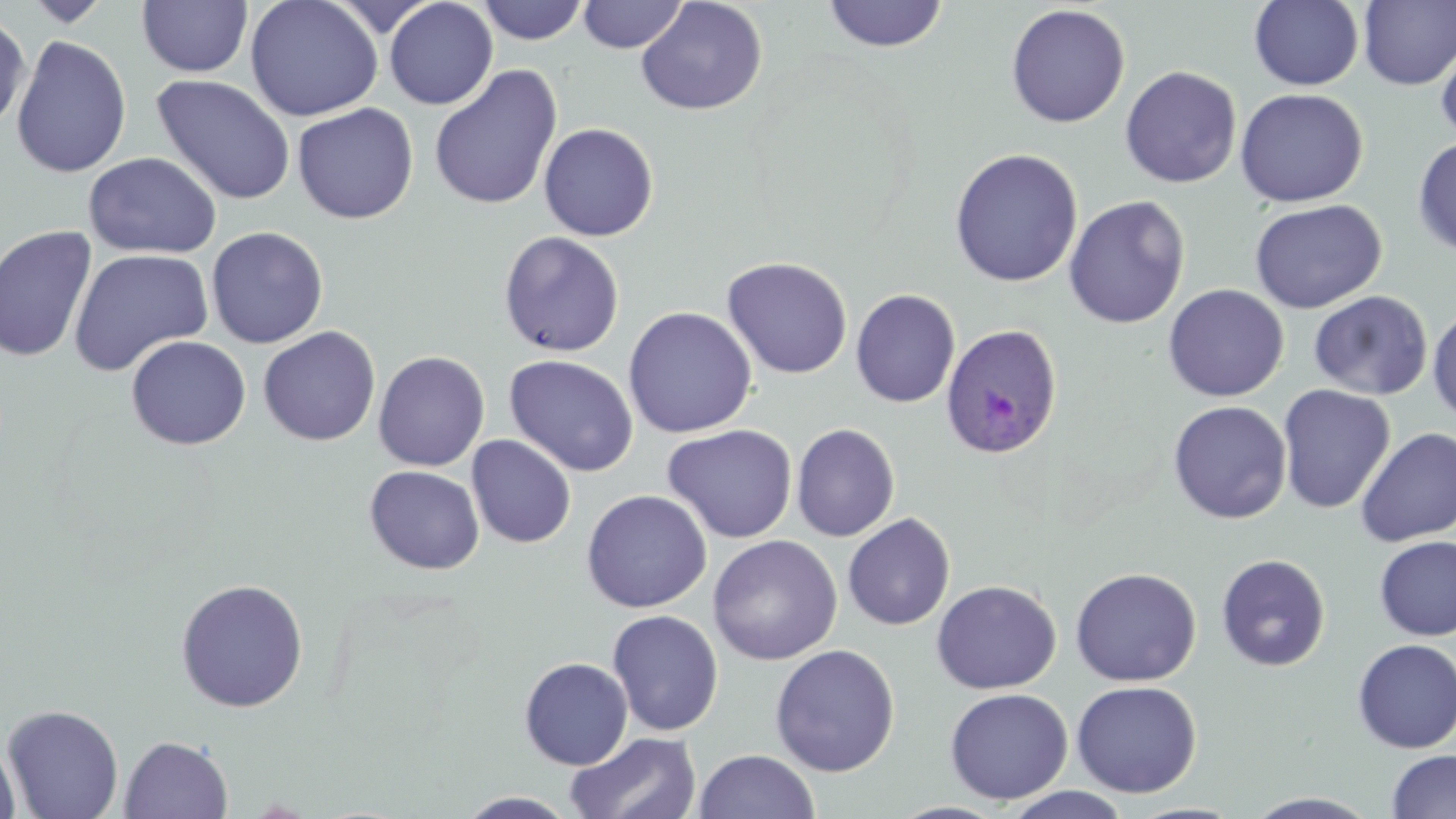
{
  "slide_level_diagnosis": "Plasmodium ovale",
  "field_of_view": "one of a larger specimen",
  "modality": "light microscopy",
  "preparation": "thin blood smear",
  "image_size": "1456×819 pixels",
  "stain": "May-Grünwald-Giemsa",
  "plasmodium_ovale_infected_red_blood_cell_locations": "approximate bounding boxes as [x1, y1, x2, y2] in pixels: [940, 322, 1064, 459]",
  "uninfected_red_blood_cell_locations": "approximate bounding boxes as [x1, y1, x2, y2] in pixels: [22, 0, 114, 27], [244, 0, 383, 121], [384, 0, 498, 110], [577, 0, 688, 53], [1249, 0, 1364, 91], [137, 1, 254, 77], [476, 1, 588, 45], [636, 1, 768, 116], [820, 1, 949, 53], [1358, 1, 1456, 90], [1005, 3, 1130, 128], [0, 11, 31, 132], [1435, 30, 1456, 147], [10, 34, 133, 178], [428, 64, 563, 212], [1120, 65, 1242, 189], [151, 73, 296, 206], [1234, 87, 1368, 208], [292, 102, 419, 224], [538, 122, 659, 242], [1412, 136, 1456, 258], [948, 147, 1084, 287], [82, 152, 222, 259], [1064, 195, 1190, 329], [1248, 198, 1386, 314], [0, 225, 99, 364], [206, 226, 329, 349], [498, 231, 625, 358], [68, 248, 214, 376], [721, 257, 853, 379], [1163, 283, 1289, 402], [850, 289, 960, 408], [1308, 291, 1433, 400], [1427, 304, 1456, 426], [623, 306, 757, 437], [258, 326, 381, 446], [125, 335, 251, 450], [373, 350, 490, 471], [503, 354, 639, 477], [1277, 384, 1396, 514], [1168, 400, 1292, 524], [791, 423, 900, 542], [661, 424, 798, 543], [1355, 427, 1456, 546], [466, 435, 577, 548], [364, 465, 484, 574], [581, 489, 712, 613], [842, 512, 955, 631], [707, 534, 843, 665], [1373, 536, 1456, 641], [1216, 553, 1331, 672], [1070, 567, 1201, 687], [174, 578, 309, 712], [930, 579, 1062, 694], [606, 609, 724, 736], [1352, 638, 1456, 754], [769, 643, 900, 777], [519, 657, 633, 770], [1071, 680, 1202, 798], [944, 687, 1073, 805], [2, 703, 124, 819], [564, 731, 704, 819], [119, 734, 233, 818], [0, 738, 21, 819], [692, 749, 820, 819], [1386, 749, 1456, 818], [1002, 787, 1135, 818], [455, 791, 583, 818]",
  "magnification": "1000x"
}